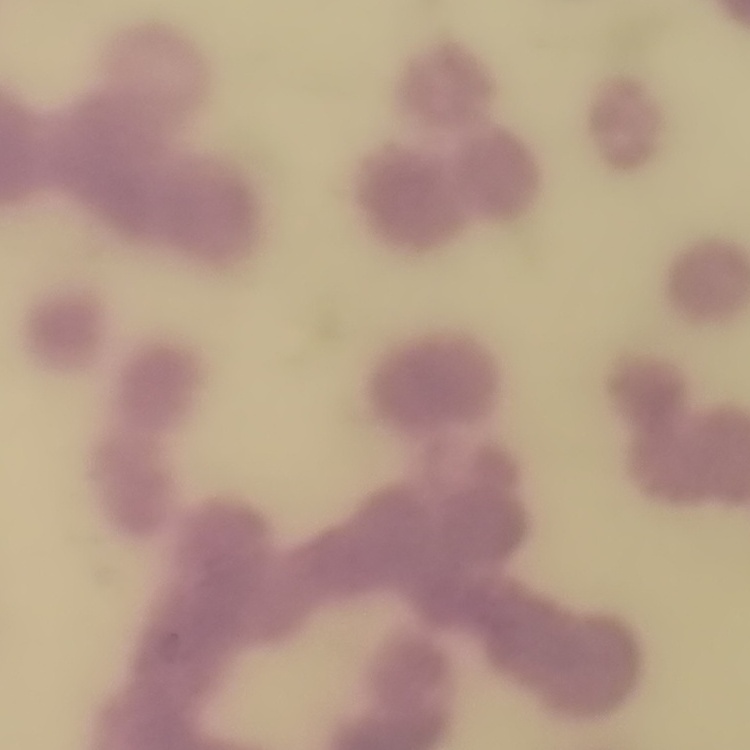

The red blood cells exhibit rouleaux formation. Stained with either Field's or Giemsa. One tile cut from a larger photomicrograph. Thin peripheral smear.